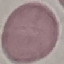

Result: no malaria parasites detected. Thin blood film. Giemsa stain. Photographed with a smartphone camera at the microscope eyepiece. Cell patch, automatically extracted from a larger field of view and resized to 64 × 64 pixels.